Outline each blood parasite and name the species.
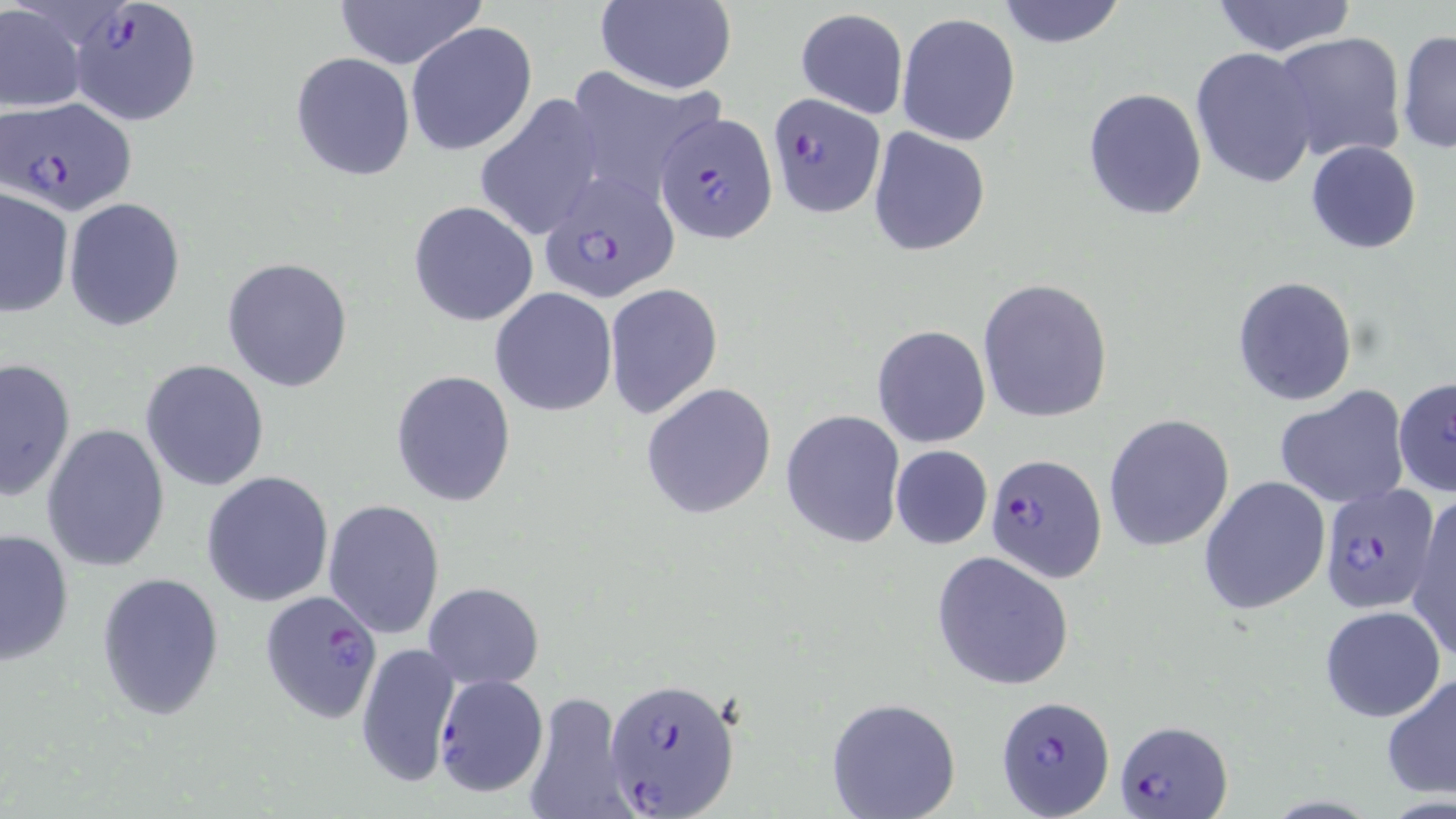
Approximate bounding boxes as named x1/y1/x2/y2 corners in pixels.
Plasmodium falciparum-infected red blood cells: (x1=68, y1=1, x2=202, y2=127), (x1=766, y1=91, x2=885, y2=217), (x1=2, y1=97, x2=137, y2=216), (x1=655, y1=110, x2=777, y2=244), (x1=537, y1=172, x2=683, y2=302), (x1=985, y1=452, x2=1108, y2=583), (x1=1319, y1=483, x2=1440, y2=616), (x1=259, y1=589, x2=386, y2=725), (x1=433, y1=673, x2=549, y2=797), (x1=607, y1=676, x2=742, y2=819), (x1=995, y1=696, x2=1115, y2=819), (x1=1114, y1=719, x2=1232, y2=817).
No Plasmodium ovale, Plasmodium malariae, Plasmodium vivax, Babesia divergens, or Trypanosoma brucei observed.

Uninfected red blood cell locations: (x1=334, y1=0, x2=483, y2=71), (x1=593, y1=0, x2=736, y2=94), (x1=994, y1=0, x2=1129, y2=50), (x1=1207, y1=0, x2=1358, y2=58), (x1=0, y1=2, x2=87, y2=115), (x1=795, y1=8, x2=909, y2=120), (x1=896, y1=12, x2=1021, y2=146), (x1=405, y1=22, x2=536, y2=157), (x1=1397, y1=29, x2=1456, y2=158), (x1=1271, y1=31, x2=1407, y2=163), (x1=1190, y1=47, x2=1319, y2=189), (x1=290, y1=53, x2=416, y2=180), (x1=561, y1=70, x2=722, y2=203), (x1=1082, y1=88, x2=1207, y2=219), (x1=474, y1=95, x2=607, y2=241), (x1=867, y1=127, x2=990, y2=256), (x1=1305, y1=140, x2=1423, y2=254), (x1=0, y1=187, x2=73, y2=317), (x1=64, y1=197, x2=185, y2=330), (x1=410, y1=200, x2=538, y2=326), (x1=222, y1=257, x2=354, y2=393), (x1=1232, y1=275, x2=1358, y2=405), (x1=976, y1=279, x2=1113, y2=422), (x1=603, y1=283, x2=723, y2=419), (x1=490, y1=289, x2=617, y2=414), (x1=871, y1=325, x2=991, y2=449), (x1=0, y1=357, x2=76, y2=503), (x1=140, y1=360, x2=270, y2=492), (x1=390, y1=369, x2=517, y2=508), (x1=1393, y1=375, x2=1456, y2=499), (x1=641, y1=382, x2=777, y2=520), (x1=1273, y1=387, x2=1411, y2=510), (x1=780, y1=408, x2=906, y2=549), (x1=1104, y1=414, x2=1235, y2=551), (x1=41, y1=423, x2=171, y2=573), (x1=889, y1=444, x2=993, y2=550), (x1=202, y1=471, x2=334, y2=608), (x1=1198, y1=475, x2=1331, y2=615), (x1=1407, y1=494, x2=1455, y2=663), (x1=323, y1=499, x2=447, y2=637), (x1=0, y1=525, x2=74, y2=668), (x1=931, y1=551, x2=1076, y2=690), (x1=97, y1=571, x2=224, y2=720), (x1=422, y1=581, x2=545, y2=689), (x1=1320, y1=605, x2=1447, y2=721), (x1=355, y1=639, x2=462, y2=789), (x1=1381, y1=672, x2=1456, y2=802), (x1=520, y1=690, x2=635, y2=819), (x1=825, y1=697, x2=962, y2=819). Slide-level diagnosis: Plasmodium falciparum. Thin blood smear. Optical microscopy. May-Grünwald-Giemsa stain. Single field of view. Image is 1456×819 pixels. Captured at 1000x magnification.